Report the malaria status of this cell.
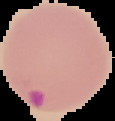

It is parasitized.

preparation: thin blood film
image_type: segmented cell region with the area outside set to black
image_size: 115×121 pixels